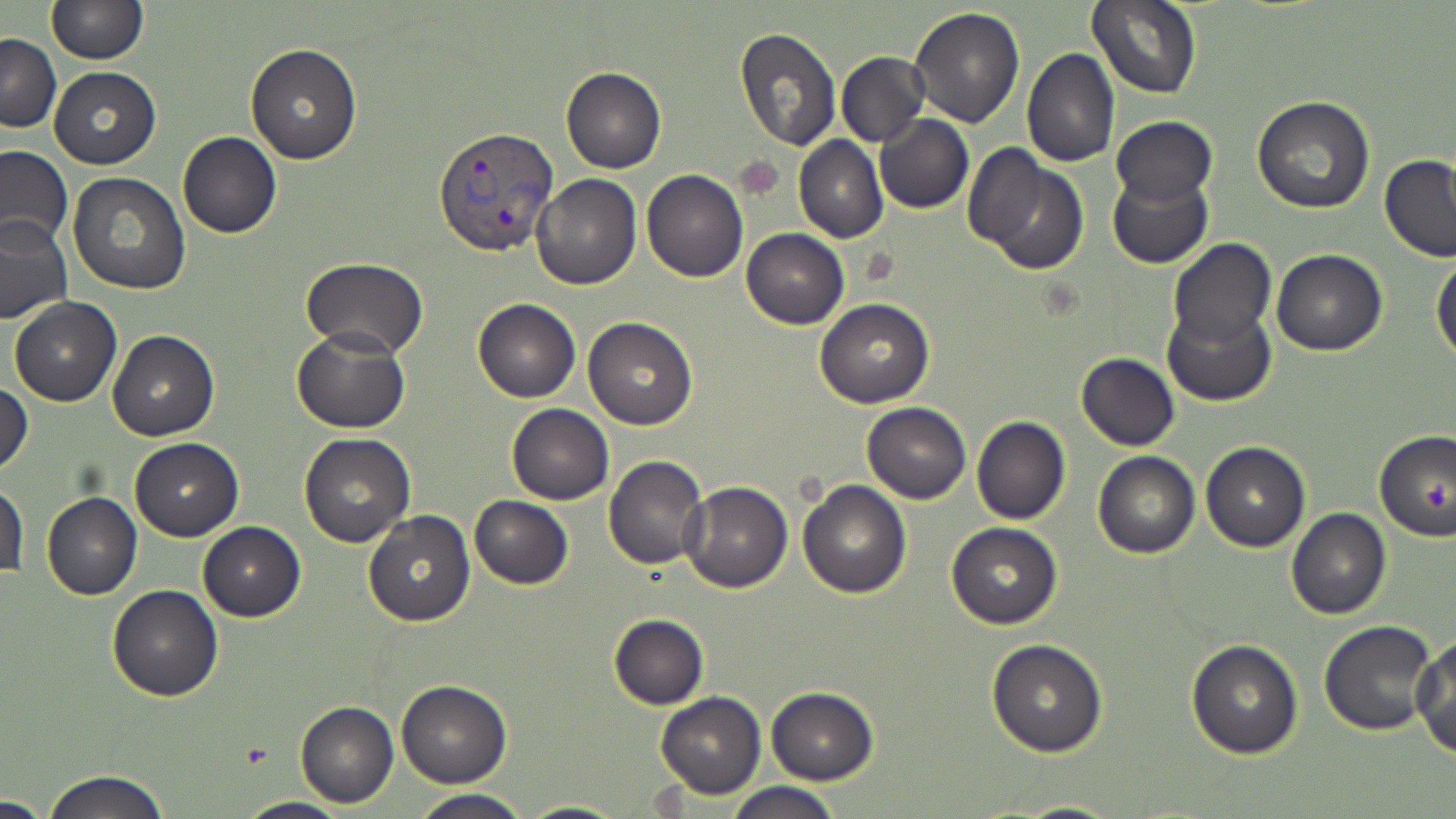 Approximate bounding boxes as [x1, y1, x2, y2] in pixels. Plasmodium vivax-infected red blood cell locations: [432, 125, 560, 257]. Platelet locations: [735, 158, 784, 199], [1423, 477, 1450, 512]. Uninfected red blood cell locations: [1086, 0, 1200, 99], [48, 1, 145, 63], [909, 7, 1027, 129], [733, 27, 842, 149], [0, 34, 61, 132], [245, 45, 361, 163], [1021, 48, 1119, 166], [835, 51, 931, 148], [49, 66, 160, 167], [561, 67, 666, 174], [1252, 95, 1376, 213], [874, 114, 973, 213], [1110, 116, 1216, 206], [178, 132, 281, 238], [795, 134, 887, 244], [0, 144, 76, 253], [971, 149, 1089, 275], [1380, 155, 1456, 262], [642, 169, 748, 281], [67, 172, 192, 294], [1107, 173, 1213, 268], [532, 174, 642, 289], [0, 216, 75, 325], [742, 228, 849, 329], [1167, 239, 1276, 351], [1271, 249, 1387, 355], [1431, 256, 1456, 365], [301, 257, 429, 361], [8, 296, 123, 406], [473, 298, 581, 402], [815, 298, 934, 408], [1163, 304, 1276, 407], [583, 317, 697, 429], [291, 328, 412, 432], [107, 330, 219, 441], [1077, 354, 1179, 450], [0, 382, 33, 479], [862, 401, 971, 503], [507, 403, 613, 504], [973, 416, 1070, 524], [299, 432, 415, 547], [1375, 433, 1455, 542], [130, 437, 242, 541], [1201, 441, 1309, 551], [1092, 451, 1201, 558], [603, 455, 708, 570], [798, 480, 911, 599], [1, 481, 28, 581], [681, 481, 792, 592], [42, 493, 143, 601], [469, 495, 573, 589], [1286, 507, 1391, 620], [362, 510, 475, 626], [198, 521, 305, 619], [946, 523, 1062, 629], [107, 583, 224, 702], [609, 613, 708, 709], [1319, 621, 1438, 736], [1412, 635, 1456, 758], [987, 638, 1108, 757], [1185, 638, 1304, 758], [395, 679, 511, 787], [765, 687, 878, 784], [656, 691, 766, 799], [295, 701, 398, 808], [42, 770, 173, 819], [728, 781, 842, 819], [410, 789, 530, 819], [0, 795, 57, 817], [234, 797, 351, 818], [995, 798, 1134, 818], [517, 799, 632, 818]. Slide-level diagnosis: Plasmodium vivax. Image is 1456×819 pixels. 1000x magnification. Thin blood film. May-Grünwald-Giemsa stain. Light microscopy. Single field of view.